Classify this cell by malaria status.
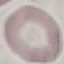

It is uninfected.

Cell patch, automatically extracted from a larger field of view and resized to 64 × 64 pixels. Thin blood smear. Giemsa-stained preparation. Acquired by smartphone through the microscope eyepiece.